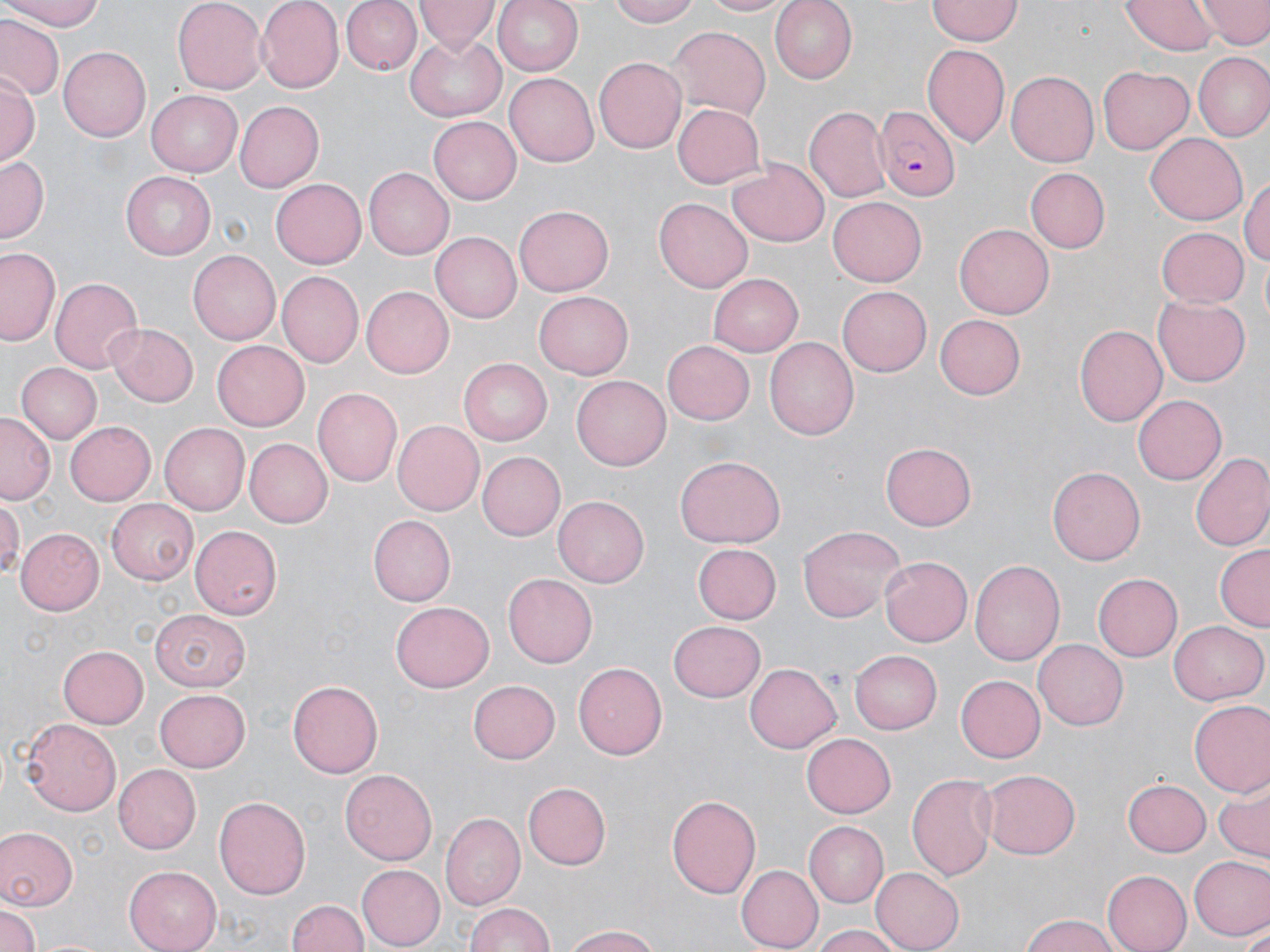

Summary:
  - Coordinate format: approximate bounding boxes as named x1/y1/x2/y2 corners in pixels
  - Plasmodium falciparum-infected red blood cell locations: (x1=870, y1=109, x2=961, y2=199)
  - Uninfected red blood cell locations: (x1=0, y1=0, x2=112, y2=30), (x1=172, y1=0, x2=265, y2=94), (x1=255, y1=0, x2=343, y2=91), (x1=417, y1=0, x2=497, y2=52), (x1=492, y1=0, x2=583, y2=78), (x1=610, y1=0, x2=704, y2=26), (x1=695, y1=0, x2=791, y2=17), (x1=771, y1=0, x2=858, y2=83), (x1=928, y1=0, x2=1022, y2=44), (x1=1121, y1=0, x2=1216, y2=55), (x1=1200, y1=0, x2=1269, y2=48), (x1=343, y1=1, x2=422, y2=75), (x1=2, y1=17, x2=63, y2=99), (x1=669, y1=26, x2=769, y2=120), (x1=405, y1=36, x2=505, y2=121), (x1=922, y1=45, x2=1010, y2=147), (x1=57, y1=46, x2=149, y2=141), (x1=1195, y1=51, x2=1270, y2=142), (x1=594, y1=56, x2=688, y2=154), (x1=1097, y1=66, x2=1194, y2=154), (x1=1006, y1=71, x2=1099, y2=168), (x1=1, y1=73, x2=38, y2=169), (x1=504, y1=73, x2=597, y2=168), (x1=146, y1=89, x2=242, y2=177), (x1=235, y1=100, x2=324, y2=192), (x1=672, y1=103, x2=766, y2=189), (x1=804, y1=106, x2=893, y2=205), (x1=428, y1=117, x2=521, y2=205), (x1=1145, y1=133, x2=1248, y2=226), (x1=0, y1=157, x2=47, y2=240), (x1=728, y1=162, x2=828, y2=246), (x1=364, y1=168, x2=454, y2=259), (x1=1026, y1=168, x2=1109, y2=253), (x1=119, y1=172, x2=214, y2=259), (x1=1242, y1=174, x2=1270, y2=273), (x1=270, y1=180, x2=364, y2=272), (x1=828, y1=197, x2=928, y2=286), (x1=655, y1=199, x2=752, y2=292), (x1=515, y1=204, x2=613, y2=293), (x1=955, y1=223, x2=1055, y2=319), (x1=1155, y1=225, x2=1248, y2=307), (x1=432, y1=231, x2=526, y2=322), (x1=1, y1=247, x2=62, y2=348), (x1=187, y1=250, x2=279, y2=345), (x1=278, y1=272, x2=363, y2=367), (x1=708, y1=272, x2=802, y2=356), (x1=50, y1=275, x2=143, y2=374), (x1=836, y1=283, x2=931, y2=373), (x1=359, y1=286, x2=453, y2=378), (x1=534, y1=291, x2=633, y2=378), (x1=1152, y1=297, x2=1250, y2=387), (x1=932, y1=313, x2=1027, y2=402), (x1=107, y1=323, x2=199, y2=406), (x1=1074, y1=324, x2=1167, y2=428), (x1=765, y1=337, x2=858, y2=441), (x1=663, y1=340, x2=754, y2=425), (x1=212, y1=341, x2=309, y2=430), (x1=459, y1=357, x2=555, y2=445), (x1=15, y1=362, x2=101, y2=444), (x1=573, y1=373, x2=670, y2=469), (x1=312, y1=388, x2=401, y2=488), (x1=1133, y1=394, x2=1226, y2=485), (x1=0, y1=413, x2=54, y2=503), (x1=392, y1=421, x2=485, y2=515), (x1=66, y1=422, x2=156, y2=504), (x1=161, y1=422, x2=250, y2=515), (x1=247, y1=437, x2=334, y2=527), (x1=880, y1=442, x2=976, y2=531), (x1=477, y1=452, x2=565, y2=540), (x1=1190, y1=452, x2=1270, y2=554), (x1=673, y1=456, x2=785, y2=549), (x1=1049, y1=464, x2=1147, y2=565), (x1=0, y1=495, x2=24, y2=582), (x1=553, y1=495, x2=649, y2=592), (x1=107, y1=499, x2=199, y2=585), (x1=370, y1=514, x2=459, y2=607), (x1=798, y1=524, x2=905, y2=623), (x1=192, y1=526, x2=282, y2=619), (x1=15, y1=528, x2=102, y2=616), (x1=691, y1=543, x2=781, y2=625), (x1=1215, y1=544, x2=1270, y2=631), (x1=879, y1=556, x2=972, y2=647), (x1=969, y1=557, x2=1063, y2=667), (x1=1091, y1=573, x2=1182, y2=662), (x1=501, y1=574, x2=595, y2=666), (x1=391, y1=602, x2=494, y2=690), (x1=150, y1=607, x2=247, y2=690), (x1=669, y1=620, x2=766, y2=703), (x1=1168, y1=620, x2=1267, y2=705), (x1=1033, y1=640, x2=1129, y2=731), (x1=58, y1=643, x2=149, y2=727), (x1=850, y1=649, x2=941, y2=734), (x1=573, y1=661, x2=669, y2=760), (x1=743, y1=661, x2=841, y2=754), (x1=957, y1=673, x2=1045, y2=763), (x1=468, y1=678, x2=560, y2=763), (x1=288, y1=679, x2=384, y2=778), (x1=155, y1=689, x2=251, y2=772), (x1=1188, y1=701, x2=1270, y2=797), (x1=21, y1=717, x2=123, y2=815), (x1=802, y1=731, x2=896, y2=815), (x1=115, y1=765, x2=201, y2=853), (x1=981, y1=766, x2=1081, y2=859), (x1=341, y1=769, x2=437, y2=865), (x1=906, y1=772, x2=1000, y2=881), (x1=1124, y1=777, x2=1211, y2=856), (x1=522, y1=782, x2=609, y2=870), (x1=1213, y1=788, x2=1269, y2=861), (x1=668, y1=793, x2=761, y2=900), (x1=214, y1=796, x2=310, y2=903), (x1=439, y1=814, x2=526, y2=911), (x1=804, y1=822, x2=889, y2=908), (x1=0, y1=827, x2=76, y2=913), (x1=1189, y1=855, x2=1269, y2=942), (x1=126, y1=864, x2=224, y2=952), (x1=357, y1=864, x2=444, y2=949), (x1=737, y1=865, x2=823, y2=949), (x1=871, y1=866, x2=965, y2=951), (x1=1103, y1=871, x2=1189, y2=951), (x1=286, y1=898, x2=370, y2=951), (x1=464, y1=902, x2=558, y2=952), (x1=0, y1=904, x2=41, y2=952), (x1=1017, y1=914, x2=1125, y2=952), (x1=557, y1=922, x2=663, y2=952), (x1=810, y1=923, x2=908, y2=952), (x1=1238, y1=925, x2=1270, y2=949)
  - Slide-level diagnosis: Plasmodium falciparum
  - Magnification: 1000x
  - Modality: light microscopy
  - Stain: May-Grünwald-Giemsa
  - Image size: 1270×952 pixels
  - Preparation: thin blood film
  - Field of view: one of a larger specimen